Identify the cell.
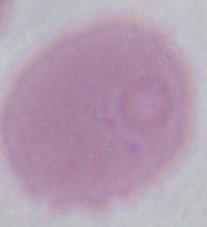
This is an erythrocyte.

1000x magnification. Photomicrograph.